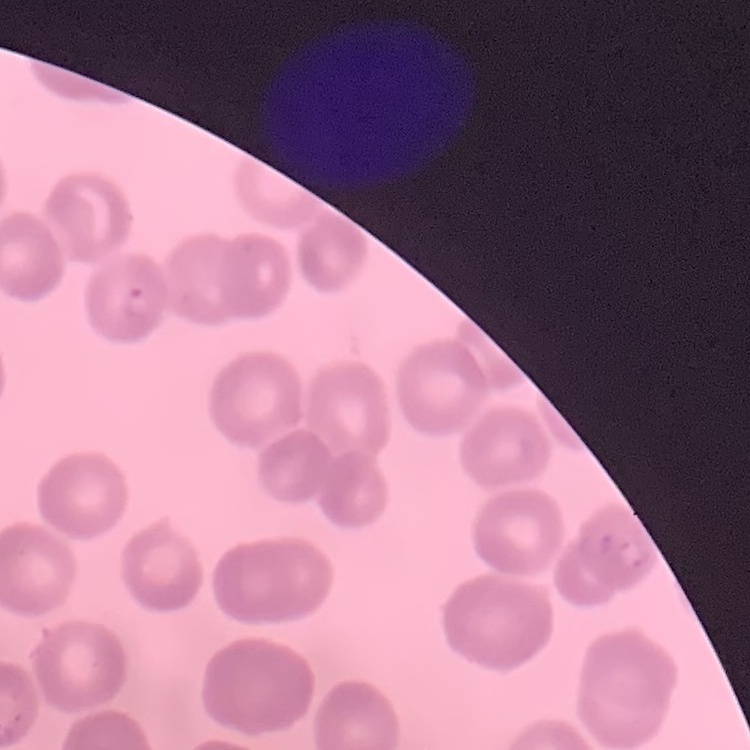
Summary:
  - Erythrocyte morphology: no rouleaux formation
  - Stain: Field's or Giemsa
  - Preparation: thin blood smear
  - Image type: one tile cut from a larger photomicrograph